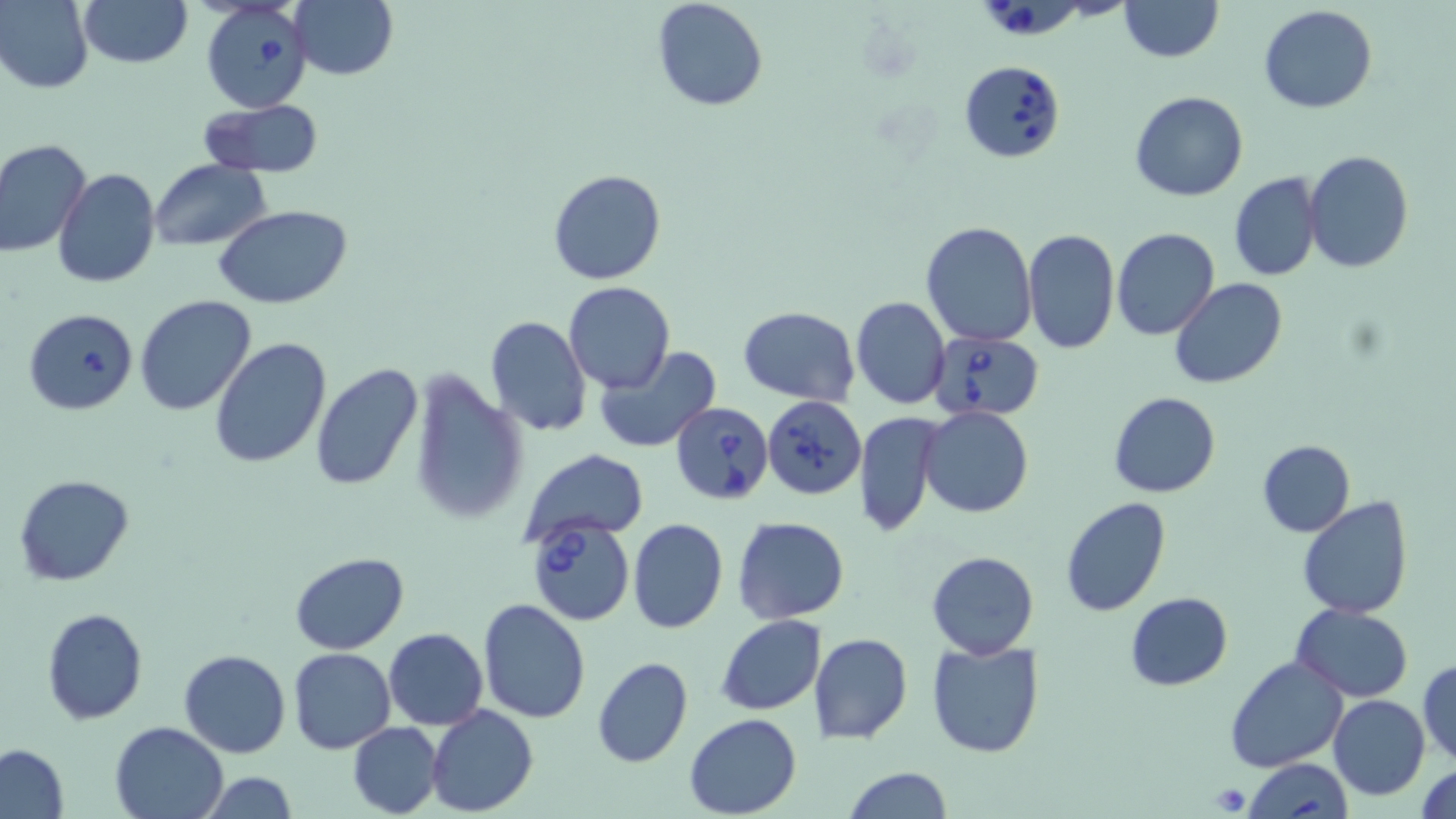

Summary:
  - Coordinate format: approximate bounding boxes as [x1, y1, x2, y2] in pixels
  - Babesia divergens-infected red blood cell locations: [982, 0, 1078, 39], [200, 2, 312, 112], [957, 60, 1065, 164], [927, 330, 1044, 421], [763, 398, 866, 503], [670, 400, 775, 505], [526, 514, 635, 626]
  - Uninfected red blood cell locations: [0, 0, 94, 93], [77, 0, 193, 69], [651, 0, 769, 112], [1118, 0, 1223, 62], [288, 1, 399, 81], [1258, 6, 1379, 113], [1130, 89, 1248, 203], [199, 99, 325, 179], [0, 138, 92, 258], [1303, 150, 1414, 274], [151, 159, 272, 251], [52, 168, 160, 289], [548, 168, 667, 285], [1229, 172, 1323, 282], [214, 204, 352, 310], [919, 222, 1037, 347], [1022, 228, 1119, 356], [1111, 228, 1220, 341], [1170, 278, 1287, 388], [564, 281, 673, 393], [134, 295, 257, 416], [850, 296, 950, 410], [738, 304, 860, 406], [22, 309, 141, 414], [484, 316, 592, 438], [209, 337, 332, 469], [594, 345, 721, 454], [310, 363, 425, 491], [408, 370, 527, 526], [1108, 392, 1222, 498], [920, 406, 1034, 517], [855, 412, 943, 537], [1256, 439, 1355, 537], [521, 448, 650, 542], [13, 474, 134, 587], [1060, 497, 1171, 618], [1297, 497, 1414, 620], [733, 517, 850, 622], [628, 519, 728, 635], [926, 551, 1038, 659], [289, 553, 410, 654], [1125, 593, 1234, 691], [477, 597, 592, 724], [1293, 605, 1413, 701], [42, 608, 148, 726], [716, 614, 826, 715], [384, 628, 488, 729], [809, 633, 912, 744], [924, 638, 1044, 760], [179, 648, 290, 758], [288, 648, 395, 754], [1225, 654, 1348, 773], [592, 657, 694, 767], [1417, 658, 1455, 767], [1327, 694, 1430, 800], [427, 706, 538, 816], [684, 713, 800, 818], [111, 720, 228, 819], [348, 722, 442, 817], [0, 745, 69, 818], [1244, 759, 1351, 818], [1416, 762, 1456, 819], [842, 767, 950, 819], [202, 770, 299, 819]
  - Platelet locations: [1208, 782, 1252, 815]
  - Slide-level diagnosis: Babesia divergens
  - Field of view: one of a larger specimen
  - Stain: May-Grünwald-Giemsa
  - Preparation: thin blood film
  - Image size: 1456×819 pixels
  - Magnification: 1000x
  - Modality: light microscopy